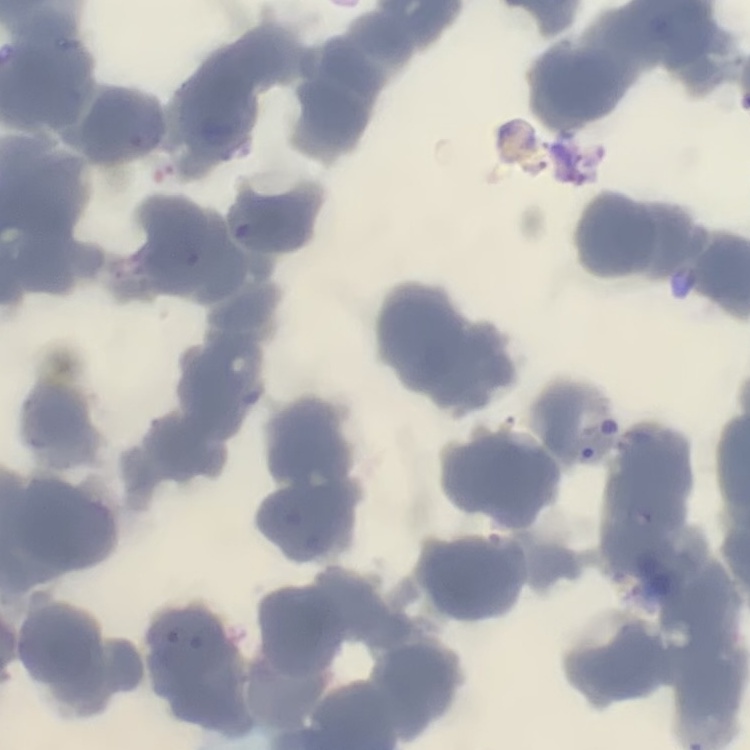
Summary:
  - Erythrocyte morphology: rouleaux formation
  - Preparation: thin peripheral smear
  - Image type: square crop of a larger photomicrograph
  - Stain: Field's or Giemsa